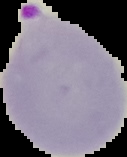
Summary:
  - Preparation: thin blood smear
  - Result: Plasmodium parasites detected
  - Image type: cell region segmented out of the field of view; surrounding area masked to black
  - Image size: 127×157 pixels